Identify the parasite.
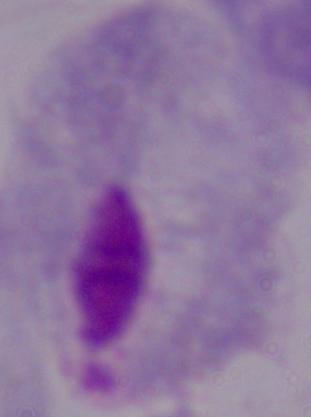

A trichomonad.

Summary:
  - Magnification: 1000x
  - Modality: photomicrograph